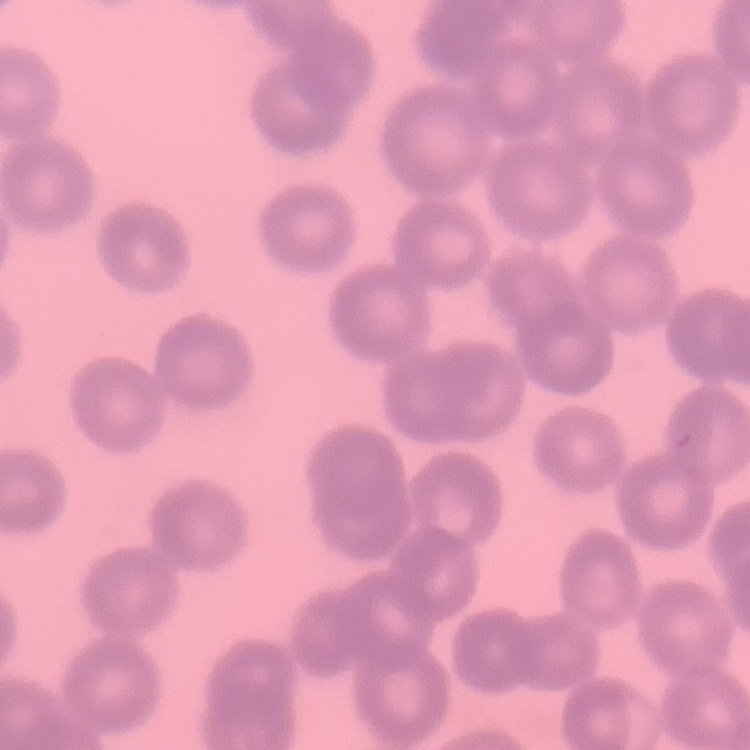

red_blood_cell_morphology: no rouleaux formation
stain: Field's or Giemsa
preparation: thin blood film
image_type: one tile cut from a larger photomicrograph